Identify the cell.
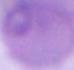

This is an erythrocyte.

{
  "modality": "micrograph",
  "magnification": "1000x"
}